Look for Plasmodium parasites.
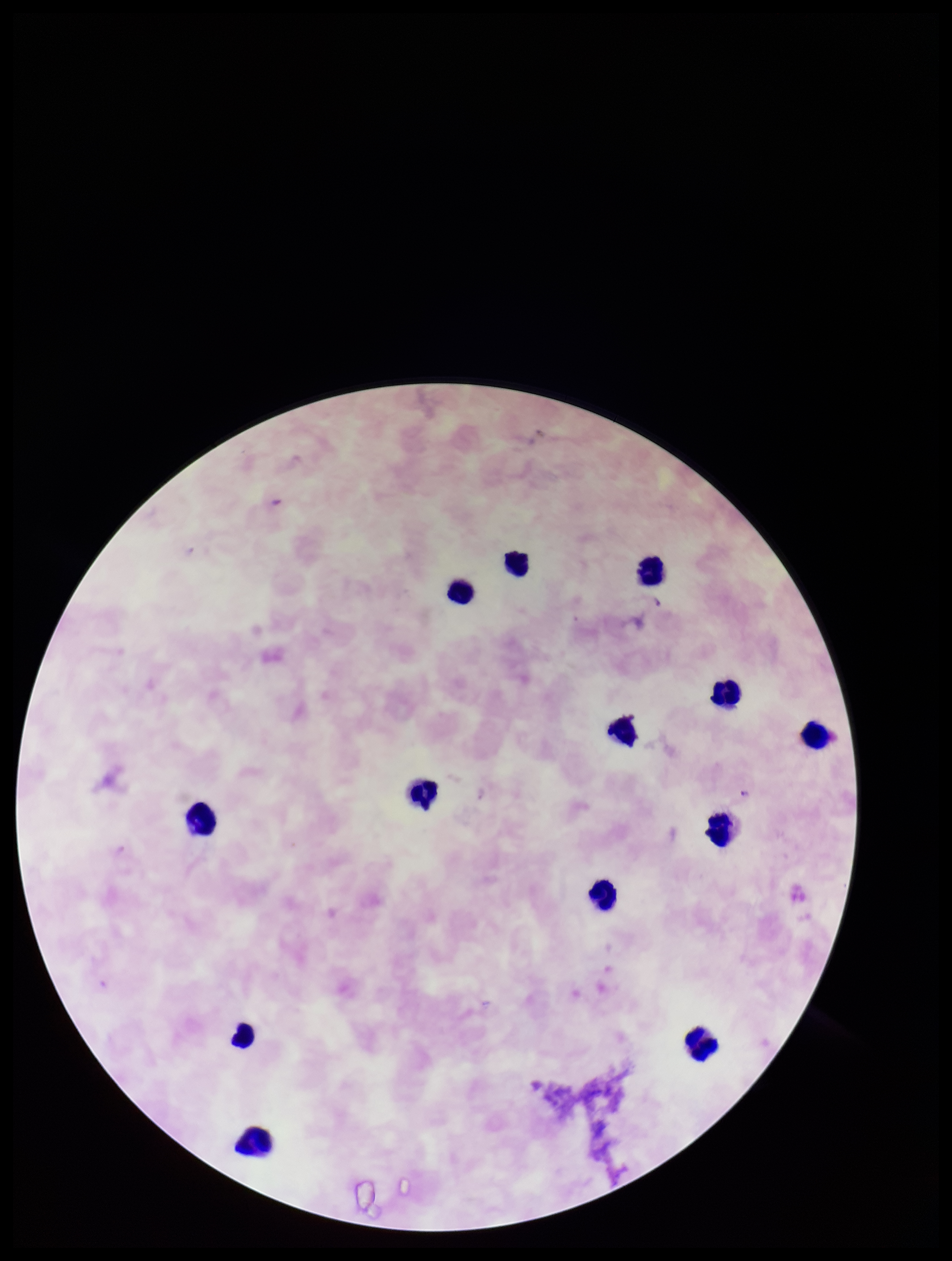
None identified.

Summary:
  - Preparation: thick
  - Stain: Giemsa
  - Leukocyte count: 13
  - Species reported for this patient: Plasmodium falciparum
  - Patient malaria status: positive
  - Parasite count: 0
  - Capture: smartphone photograph through the microscope eyepiece
  - Field of view: single
  - Image size: 952×1261 pixels